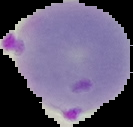

{
  "result": "malaria parasites detected",
  "preparation": "thin blood film",
  "image_type": "segmented cell region on a black background",
  "image_size": "133×127 pixels"
}